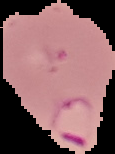
image type = segmented cell region on a black background
preparation = thin blood film
result = Plasmodium parasites detected
image size = 115×154 pixels